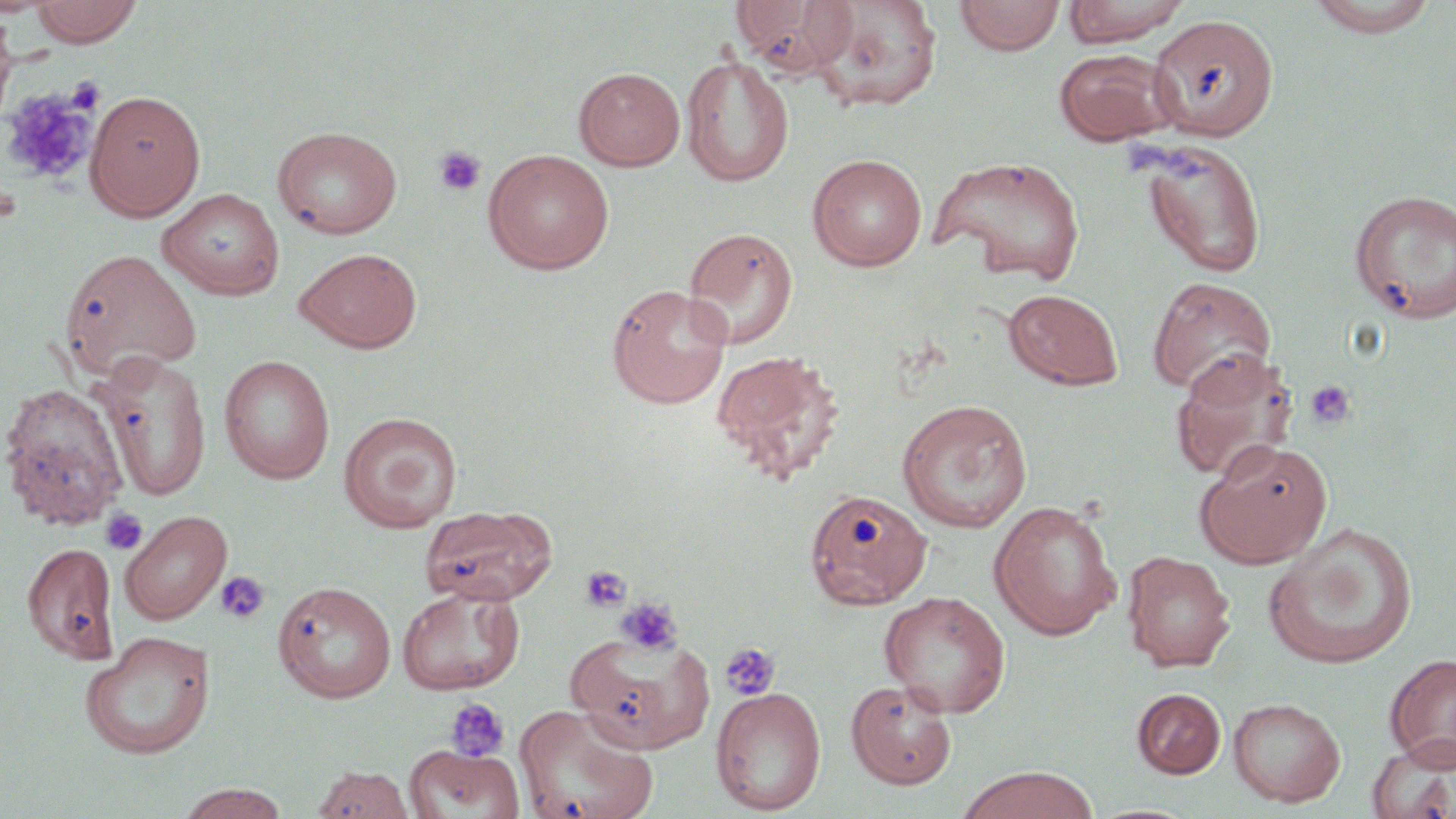
{
  "slide_level_diagnosis": "no evidence of blood parasites",
  "stain": "May-Grünwald-Giemsa",
  "uninfected_red_blood_cell_locations": "approximate bounding boxes as (x1, y1, x2, y2) in pixels: (30, 0, 144, 47), (731, 0, 858, 77), (810, 0, 943, 112), (954, 0, 1065, 56), (1062, 0, 1190, 47), (1306, 0, 1441, 37), (0, 9, 19, 134), (1147, 13, 1279, 140), (1053, 48, 1178, 146), (681, 54, 794, 186), (574, 67, 686, 171), (85, 90, 205, 220), (272, 125, 402, 239), (1135, 138, 1269, 279), (483, 149, 614, 274), (806, 153, 928, 271), (929, 154, 1087, 286), (159, 188, 284, 300), (1350, 188, 1456, 323), (683, 226, 799, 350), (294, 247, 422, 353), (59, 249, 202, 379), (1147, 276, 1277, 397), (606, 284, 732, 408), (1003, 288, 1124, 391), (710, 350, 845, 482), (1170, 350, 1297, 484), (94, 353, 212, 502), (219, 355, 336, 485), (0, 382, 130, 531), (897, 399, 1033, 533), (339, 412, 462, 532), (1194, 440, 1332, 569), (804, 488, 932, 610), (988, 499, 1123, 640), (420, 503, 557, 604), (120, 510, 231, 624), (1263, 523, 1419, 669), (23, 541, 120, 665), (1121, 550, 1236, 671), (273, 580, 397, 703), (397, 586, 525, 695), (879, 591, 1011, 718), (566, 629, 714, 754), (79, 630, 216, 760), (1385, 653, 1456, 769), (845, 679, 957, 790), (711, 686, 827, 815), (1132, 688, 1226, 779), (1228, 697, 1347, 807), (514, 703, 658, 819), (1366, 735, 1456, 819), (405, 745, 524, 819), (312, 765, 414, 818), (955, 766, 1100, 819), (174, 783, 291, 819)",
  "preparation": "thin blood film",
  "modality": "light microscopy",
  "platelet_locations": "approximate bounding boxes as (x1, y1, x2, y2) in pixels: (67, 77, 104, 114), (2, 87, 96, 184), (434, 145, 487, 197), (1303, 380, 1357, 431), (101, 508, 147, 555), (580, 565, 632, 612), (214, 569, 270, 624), (614, 597, 683, 656), (719, 641, 781, 702), (444, 698, 510, 763)",
  "field_of_view": "single",
  "magnification": "1000x",
  "image_size": "1456×819 pixels"
}